Outline each Plasmodium vivax-infected red blood cell.
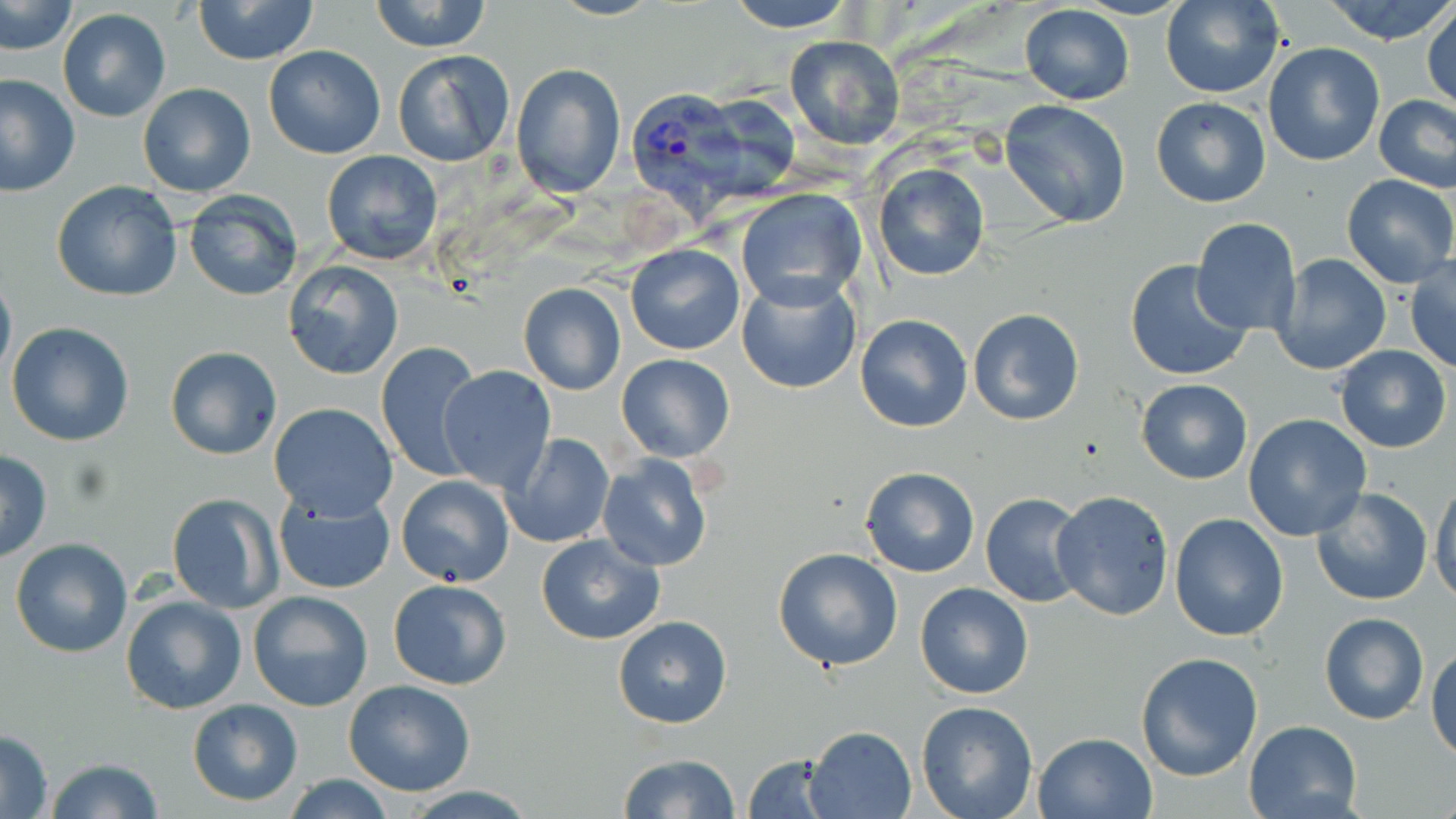

Approximate bounding boxes as [x1, y1, x2, y2] in pixels.
Plasmodium vivax-infected red blood cells: [628, 87, 740, 196].

Summary:
  - Uninfected red blood cell locations: [192, 0, 321, 65], [368, 0, 494, 53], [720, 0, 863, 32], [1159, 0, 1286, 99], [1326, 0, 1456, 46], [1, 1, 76, 54], [1019, 4, 1134, 105], [1423, 6, 1455, 113], [58, 8, 171, 122], [784, 34, 906, 150], [1262, 42, 1385, 167], [262, 45, 386, 160], [391, 49, 515, 168], [512, 63, 626, 197], [1, 73, 78, 196], [137, 83, 256, 197], [689, 92, 804, 197], [1375, 94, 1456, 191], [1150, 97, 1272, 207], [1000, 99, 1130, 228], [322, 149, 443, 266], [873, 163, 990, 281], [1342, 174, 1455, 287], [51, 183, 183, 300], [735, 188, 866, 309], [182, 191, 303, 304], [1190, 218, 1303, 336], [1190, 234, 1384, 358], [625, 244, 744, 355], [1272, 253, 1391, 377], [1406, 256, 1456, 373], [1124, 258, 1254, 383], [284, 261, 403, 380], [0, 267, 15, 385], [734, 272, 862, 394], [518, 283, 627, 396], [968, 308, 1084, 425], [855, 314, 973, 433], [5, 322, 135, 447], [375, 340, 486, 481], [1334, 344, 1452, 453], [164, 345, 282, 460], [616, 354, 736, 463], [437, 367, 557, 493], [1136, 379, 1253, 484], [268, 402, 399, 521], [1242, 413, 1372, 542], [500, 433, 614, 549], [0, 450, 52, 562], [597, 453, 715, 573], [860, 467, 980, 578], [396, 474, 515, 588], [1430, 479, 1456, 606], [272, 487, 398, 595], [1309, 488, 1434, 607], [1050, 490, 1175, 620], [166, 492, 281, 613], [979, 493, 1087, 607], [1170, 514, 1290, 642], [535, 533, 665, 645], [9, 537, 134, 658], [772, 547, 904, 672], [387, 578, 512, 691], [915, 583, 1035, 699], [248, 591, 375, 712], [120, 595, 247, 716], [1319, 613, 1430, 725], [612, 615, 734, 730], [1427, 641, 1456, 762], [1134, 650, 1264, 781], [342, 680, 478, 798], [187, 699, 304, 805], [916, 701, 1039, 819], [1244, 720, 1363, 819], [806, 727, 916, 818], [0, 729, 55, 817], [1033, 730, 1158, 819], [618, 753, 742, 819], [743, 754, 835, 818], [41, 758, 165, 818], [281, 775, 400, 818], [397, 786, 539, 818]
  - Slide-level diagnosis: Plasmodium vivax
  - Modality: light microscopy
  - Image size: 1456×819 pixels
  - Stain: May-Grünwald-Giemsa
  - Preparation: thin blood smear
  - Field of view: one of a larger specimen
  - Magnification: 1000x